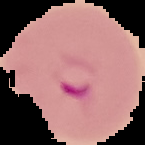
{
  "image_type": "segmented cell region with the area outside set to black",
  "result": "malaria parasites detected",
  "image_size": "145×145 pixels",
  "preparation": "thin blood film"
}